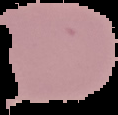

image size = 118×115 pixels
image type = segmented cell region with the area outside set to black
preparation = thin blood film
malaria status = uninfected